Give the position of every Plasmodium parasite visible.
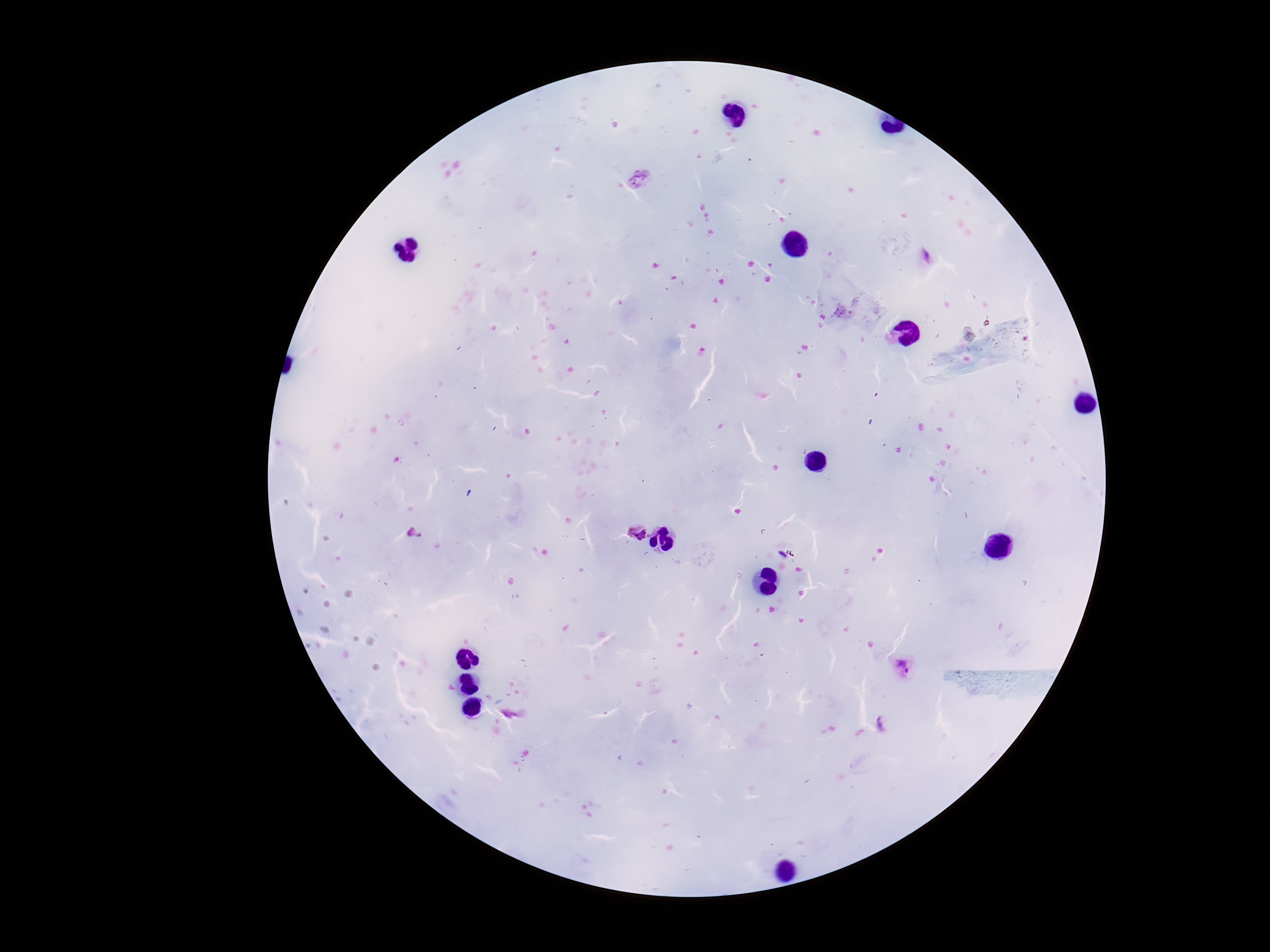

Approximate centers as (x, y) in pixels.
Plasmodium parasites: (639, 180), (633, 532), (903, 664).

{
  "magnification": "100x",
  "field_of_view": "single",
  "stain": "Giemsa",
  "capture": "smartphone camera through the microscope eyepiece",
  "preparation": "thick blood smear",
  "patient_malaria_status": "positive",
  "image_size": "1270×952 pixels"
}